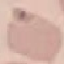

result = no malaria parasites detected
preparation = thin blood film
capture = smartphone camera at the microscope eyepiece
image type = automatically extracted cell patch, resized to 64 × 64 pixels
stain = Giemsa